Locate every blood parasite and identify its species.
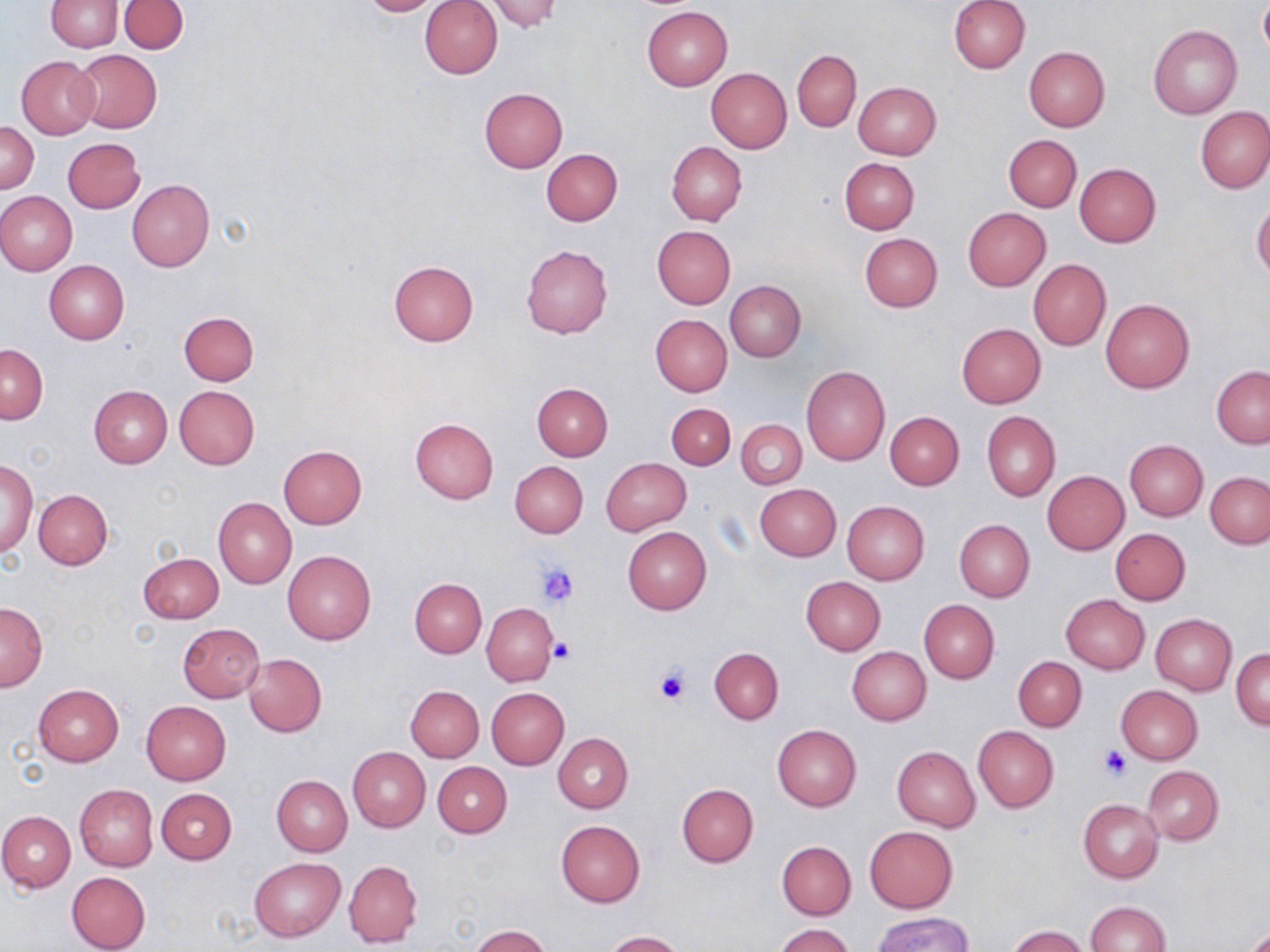
No blood parasites seen.

Approximate bounding boxes as (x1, y1, x2, y2) in pixels. Uninfected red blood cell locations: (356, 0, 447, 16), (419, 0, 502, 79), (949, 0, 1029, 73), (46, 1, 122, 52), (119, 1, 188, 54), (483, 1, 567, 33), (1258, 3, 1269, 58), (642, 5, 732, 90), (1148, 24, 1242, 120), (1024, 47, 1110, 131), (73, 50, 160, 132), (792, 50, 861, 131), (17, 56, 100, 138), (706, 68, 792, 152), (852, 81, 942, 160), (479, 87, 568, 173), (1195, 106, 1270, 193), (1, 120, 40, 193), (1004, 134, 1082, 212), (63, 138, 146, 213), (666, 142, 747, 225), (542, 149, 622, 225), (839, 157, 919, 234), (1073, 163, 1161, 248), (127, 180, 214, 271), (1, 191, 77, 276), (1252, 200, 1270, 280), (962, 208, 1051, 291), (653, 226, 736, 308), (859, 233, 943, 312), (521, 244, 613, 339), (1028, 259, 1111, 350), (43, 260, 129, 345), (387, 261, 477, 347), (725, 281, 805, 362), (1101, 299, 1194, 392), (178, 311, 258, 385), (651, 314, 732, 395), (956, 323, 1046, 407), (1, 345, 48, 423), (801, 366, 889, 466), (1211, 366, 1270, 448), (532, 383, 613, 461), (89, 384, 172, 468), (174, 385, 259, 469), (666, 404, 735, 469), (885, 412, 964, 489), (982, 412, 1060, 501), (410, 417, 499, 505), (736, 419, 806, 490), (1124, 439, 1208, 520), (278, 445, 367, 529), (1, 458, 37, 558), (601, 458, 691, 535), (510, 461, 588, 538), (1042, 470, 1129, 554), (1206, 472, 1270, 549), (754, 483, 841, 561), (34, 489, 112, 569), (214, 497, 296, 589), (842, 502, 929, 584), (954, 519, 1035, 602), (623, 526, 712, 614), (1110, 528, 1190, 604), (283, 551, 375, 645), (137, 552, 223, 624), (801, 576, 886, 654), (410, 578, 486, 658), (1060, 594, 1149, 674), (919, 599, 1000, 683), (0, 602, 48, 690), (482, 603, 556, 685), (1150, 614, 1235, 696), (177, 623, 265, 703), (709, 647, 784, 724), (847, 647, 932, 725), (1233, 648, 1269, 731), (242, 653, 327, 738), (1013, 656, 1086, 731), (32, 684, 123, 766), (405, 685, 484, 762), (1116, 685, 1204, 764), (487, 688, 569, 769), (141, 701, 231, 785), (772, 724, 861, 811), (974, 726, 1058, 812), (553, 733, 633, 813), (892, 746, 981, 832), (347, 747, 430, 832), (433, 761, 512, 837), (1141, 765, 1224, 845), (272, 775, 352, 855), (677, 783, 759, 866), (74, 785, 158, 870), (157, 789, 236, 865), (1079, 800, 1163, 883), (0, 811, 75, 892), (555, 820, 645, 908), (864, 826, 957, 912), (776, 840, 856, 920), (249, 857, 345, 941), (344, 860, 423, 948), (66, 871, 150, 952), (1084, 901, 1171, 952), (873, 913, 974, 952), (774, 924, 854, 952), (469, 925, 550, 952), (1007, 926, 1090, 952), (602, 930, 684, 952). Platelet locations: (532, 561, 579, 607), (547, 636, 575, 665), (653, 666, 691, 706), (1099, 745, 1131, 781). Slide-level diagnosis: no evidence of blood parasites. May-Grünwald-Giemsa stain. Captured at 1000x magnification. Thin blood film. Optical microscopy. Image is 1270×952 pixels. Single field of view.